Give the position of every leukocyte visible.
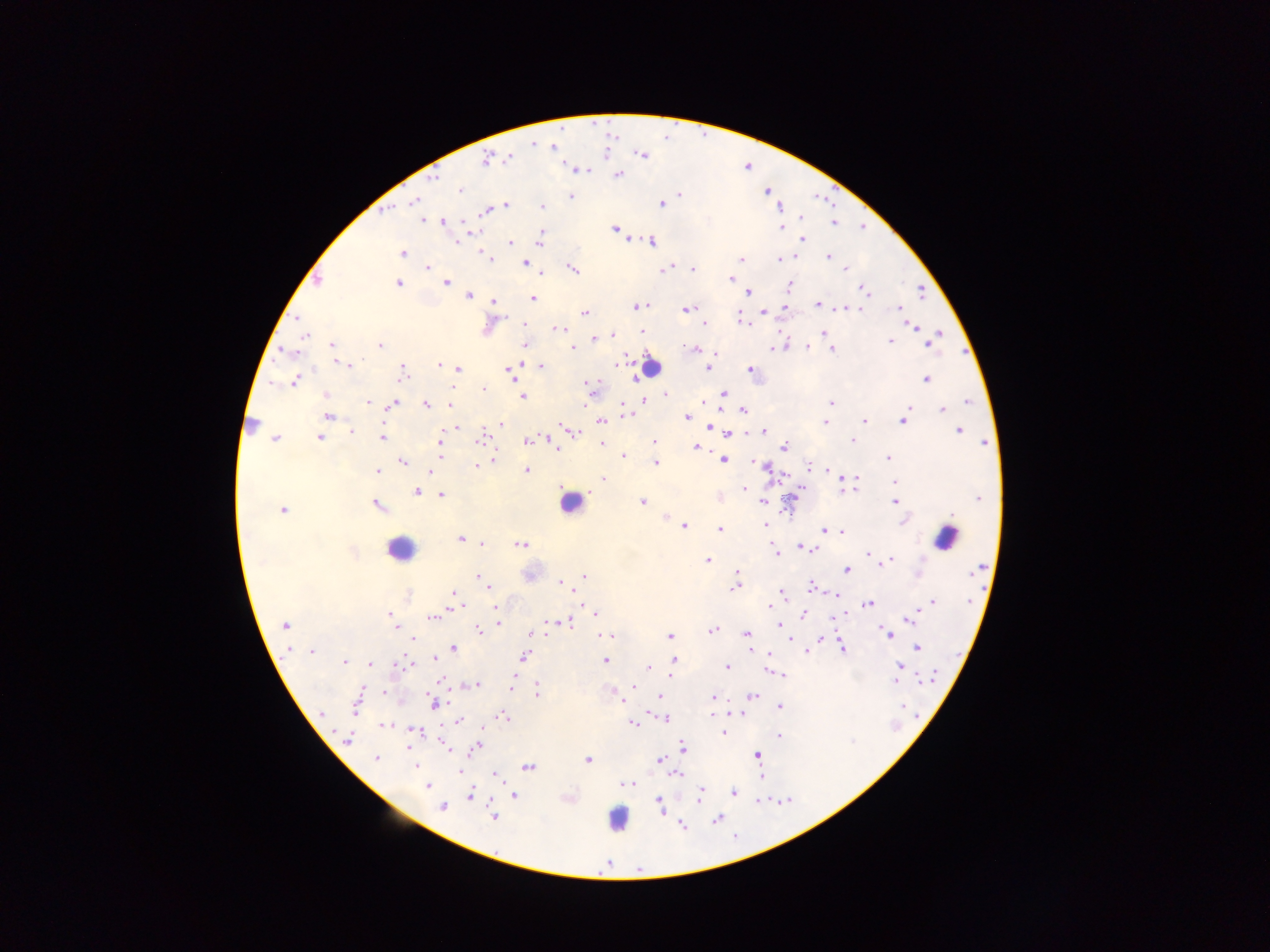
Approximate centers as [x, y] in pixels.
Leukocytes: [650, 367], [249, 422], [571, 503], [943, 536], [398, 550], [614, 816].

{
  "preparation": "thick blood film",
  "field_of_view": "single",
  "image_size": "1270×952 pixels",
  "plasmodium_parasite_locations": "approximate centers as [x, y] in pixels: [533, 144], [551, 147], [642, 155], [510, 158], [486, 159], [618, 175], [434, 177], [460, 191], [767, 192], [680, 194], [570, 196], [415, 201], [661, 204], [505, 205], [542, 207], [780, 207], [386, 210], [487, 211], [800, 217], [423, 220], [441, 222], [834, 223], [781, 227], [615, 228], [474, 231], [540, 235], [803, 239], [456, 241], [539, 241], [651, 241], [511, 242], [402, 253], [486, 256], [828, 256], [795, 257], [490, 259], [741, 259], [779, 260], [525, 262], [427, 267], [664, 269], [693, 269], [845, 269], [573, 270], [541, 274], [731, 278], [318, 280], [446, 283], [398, 284], [790, 286], [864, 289], [749, 292], [468, 295], [533, 299], [493, 301], [818, 304], [638, 306], [783, 307], [899, 308], [687, 310], [764, 311], [585, 312], [298, 318], [742, 319], [701, 320], [703, 323], [745, 323], [525, 324], [913, 326], [557, 329], [641, 332], [823, 332], [940, 334], [306, 335], [613, 336], [594, 339], [890, 342], [929, 343], [331, 345], [525, 345], [379, 346], [807, 347], [573, 348], [773, 348], [694, 349], [831, 349], [287, 353], [625, 359], [346, 365], [438, 365], [542, 366], [514, 367], [402, 368], [709, 368], [750, 368], [458, 369], [509, 372], [401, 376], [926, 379], [294, 381], [590, 386], [484, 389], [723, 394], [665, 395], [325, 396], [523, 397], [643, 399], [368, 402], [831, 402], [968, 402], [394, 404], [426, 405], [450, 406], [743, 410], [943, 410], [626, 414], [329, 416], [687, 417], [864, 420], [601, 421], [903, 421], [825, 422], [500, 424], [456, 426], [709, 426], [764, 431], [959, 431], [352, 432], [574, 432], [728, 433], [382, 436], [319, 438], [439, 438], [274, 439], [482, 440], [529, 440], [654, 441], [852, 441], [602, 444], [784, 446], [697, 447], [556, 449], [441, 455], [624, 457], [888, 459], [494, 460], [722, 460], [401, 461], [655, 464], [477, 466], [764, 466], [809, 467], [526, 470], [829, 470], [376, 471], [431, 472], [851, 478], [604, 479], [895, 482], [744, 490], [416, 492], [441, 495], [978, 497], [642, 502], [762, 502], [895, 502], [378, 506], [283, 510], [952, 515], [667, 518], [765, 525], [684, 526], [719, 528], [824, 531], [841, 532], [460, 540], [482, 544], [521, 544], [799, 546], [812, 550], [352, 552], [776, 553], [867, 554], [708, 560], [890, 560], [976, 570], [847, 571], [737, 572], [584, 575], [479, 577], [560, 583], [488, 585], [734, 587], [812, 587], [781, 592], [455, 593], [836, 595], [931, 603], [868, 604], [457, 606], [770, 606], [496, 607], [594, 613], [390, 615], [804, 615], [432, 617], [912, 619], [498, 623], [548, 623], [568, 623], [285, 625], [779, 625], [395, 627], [479, 630], [713, 630], [534, 633], [746, 633], [887, 633], [609, 635], [669, 636], [413, 639], [821, 639], [917, 647], [842, 648], [453, 649], [754, 650], [312, 651], [806, 651], [768, 654], [524, 657], [434, 658], [605, 660], [674, 660], [343, 663], [398, 664], [370, 665], [404, 665], [900, 666], [648, 667], [727, 667], [770, 670], [780, 674], [929, 677], [895, 679], [440, 680], [476, 685], [632, 686], [511, 687], [383, 691], [538, 691], [614, 693], [752, 696], [659, 697], [713, 697], [357, 702], [433, 704], [779, 706], [321, 714], [661, 715], [712, 716], [505, 717], [665, 718], [459, 721], [632, 723], [384, 727], [411, 729], [723, 733], [780, 736], [349, 740], [408, 747], [476, 747], [683, 747], [448, 749], [758, 755], [376, 759], [588, 760], [660, 760], [416, 766], [528, 767], [460, 771], [678, 775], [496, 776], [626, 783], [428, 786], [700, 792], [733, 792], [471, 795], [514, 795], [699, 798], [659, 803], [442, 807], [493, 817], [717, 819], [681, 824]",
  "capture": "mobile-phone photograph through a microscope",
  "country": "Ghana"
}